Classify the preparation.
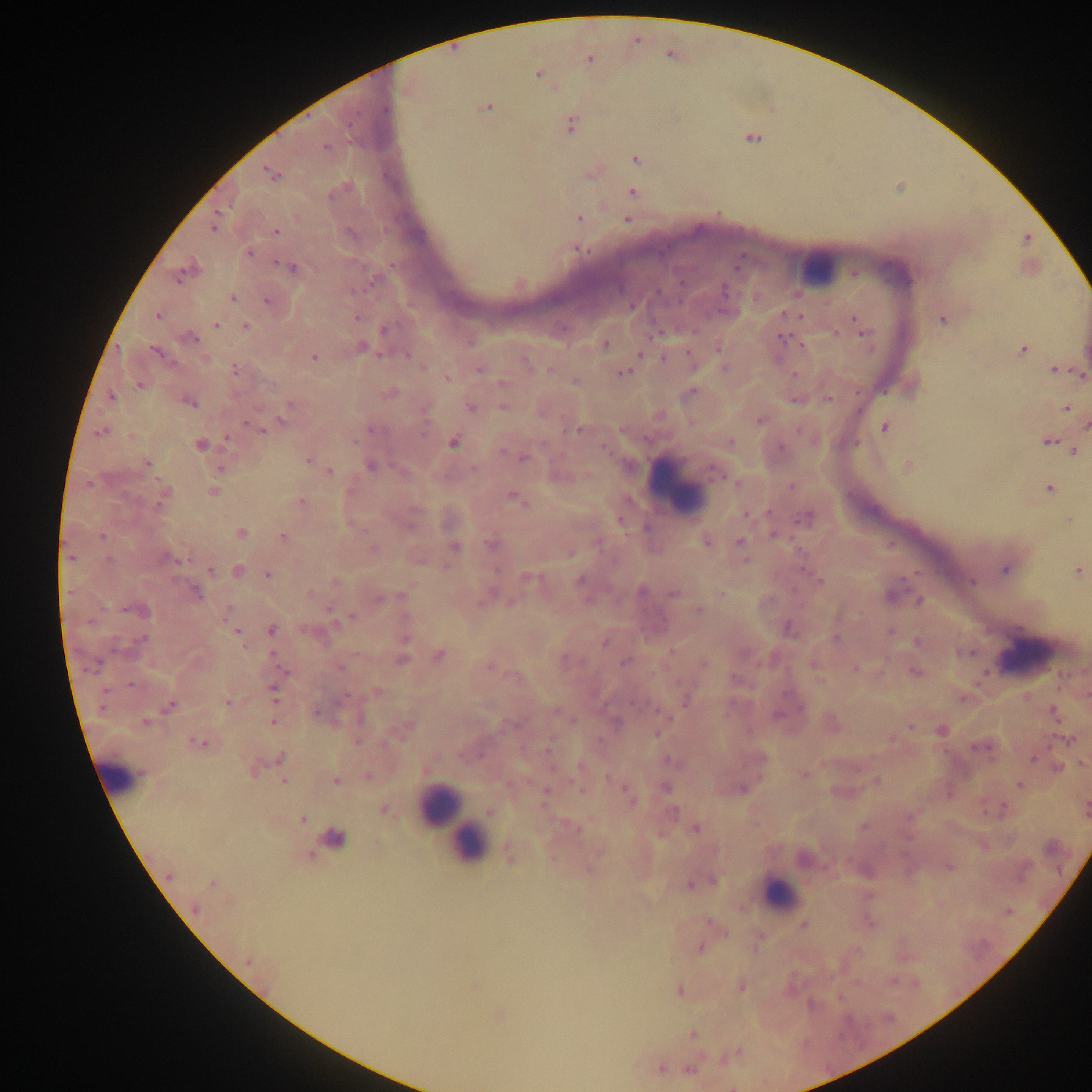
This is a thick smear.

Approximate centers as x y in pixels.
Summary:
  - Object labeled both malaria parasite and leukocyte by the source: 332 839
  - Malaria parasite locations: 636 40; 589 58; 537 73; 406 89; 485 106; 570 125; 752 137; 324 146; 636 159; 593 171; 270 173; 632 192; 578 217; 626 218; 214 224; 275 231; 1027 238; 248 253; 292 268; 185 271; 231 297; 267 301; 782 312; 158 315; 802 316; 356 317; 854 318; 943 319; 215 325; 244 326; 384 329; 834 333; 864 333; 189 337; 781 337; 604 343; 803 345; 360 347; 718 347; 1022 350; 155 352; 640 352; 314 357; 664 358; 422 365; 480 368; 1054 369; 235 370; 623 372; 1081 374; 793 375; 447 378; 575 381; 502 383; 690 391; 389 393; 827 399; 188 400; 503 405; 470 407; 1066 407; 759 420; 1085 425; 884 426; 262 429; 371 429; 580 429; 101 431; 228 439; 1047 440; 453 442; 730 443; 200 445; 604 446; 1073 450; 308 458; 522 458; 146 463; 369 465; 907 466; 220 469; 328 470; 738 482; 792 485; 1048 488; 212 492; 163 497; 515 499; 300 501; 746 514; 806 517; 1070 519; 240 533; 774 534; 102 537; 282 537; 706 541; 740 542; 491 544; 453 547; 373 548; 569 553; 745 560; 1005 568; 1077 570; 210 571; 237 571; 267 574; 527 577; 580 580; 819 581; 971 581; 335 582; 641 590; 196 593; 310 593; 672 593; 720 593; 919 601; 509 602; 136 609; 698 609; 330 611; 352 616; 227 617; 232 627; 787 627; 271 629; 890 631; 236 632; 835 638; 140 639; 605 641; 917 642; 743 652; 968 652; 438 655; 401 659; 624 661; 703 664; 488 665; 339 666; 854 668; 915 672; 984 672; 273 689; 375 692; 962 698; 685 700; 229 702; 169 706; 315 712; 1053 712; 273 721; 146 722; 911 725; 404 729; 941 729; 657 733; 890 738; 356 740; 1070 740; 198 741; 547 750; 281 757; 1033 758; 667 760; 1081 763; 253 766; 579 766; 1056 768; 803 774; 367 776; 607 777; 334 780; 876 780; 283 781; 1019 784; 665 787; 582 788; 626 788; 742 789; 545 792; 629 796; 1003 807; 1085 809; 384 811; 488 812; 673 812; 302 819; 696 828; 576 829; 597 851; 509 854; 308 855; 948 866; 588 868; 713 880; 701 881; 690 883; 212 884; 740 907; 194 909; 1006 911; 710 922; 803 924; 699 948; 248 961; 473 985; 740 986; 679 990; 500 1014; 691 1034; 733 1053; 660 1068; 689 1069
  - Leukocyte locations: 817 265; 674 487; 1028 655; 117 775; 440 806; 451 825; 466 845; 779 894
  - Field of view: single
  - Country: Ghana
  - Capture: mobile-phone photograph through a microscope
  - Image size: 1092×1092 pixels